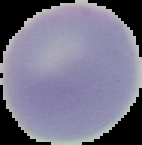
Summary:
  - Image type: segmented cell region on a black background
  - Result: no Plasmodium parasites seen
  - Preparation: thin blood film
  - Image size: 142×145 pixels